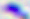

Toxoplasma gondii is seen. Photomicrograph. 400x magnification.